Outline each blood parasite and name the species.
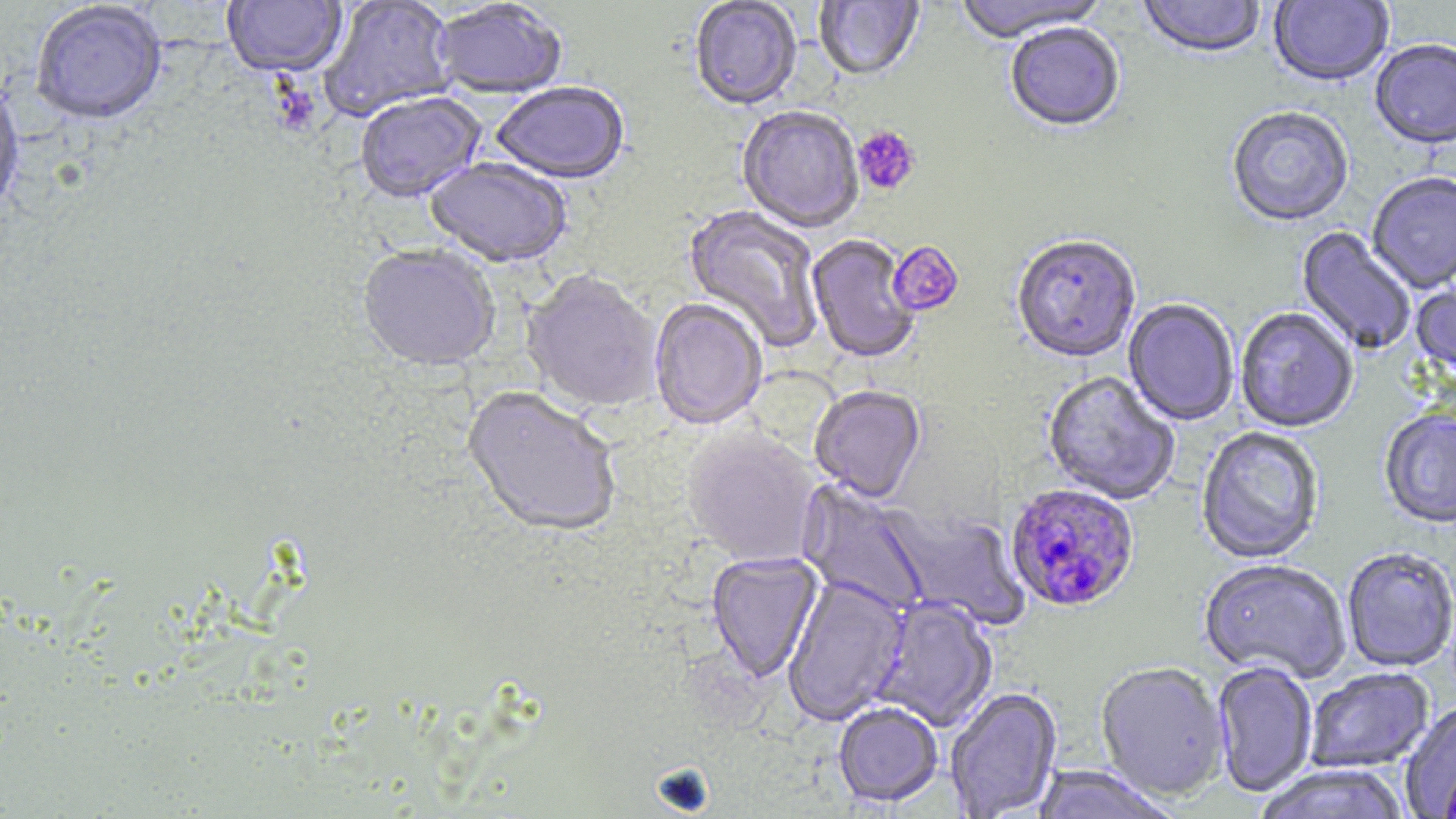

Approximate bounding boxes as (x1, y1, x2, y2) in pixels.
Plasmodium falciparum-infected red blood cells: (1004, 485, 1139, 613).
No Plasmodium ovale, Plasmodium malariae, Plasmodium vivax, Babesia divergens, or Trypanosoma brucei observed.

{
  "slide_level_diagnosis": "Plasmodium falciparum",
  "stain": "May-Grünwald-Giemsa",
  "modality": "optical microscopy",
  "platelet_locations": "approximate bounding boxes as (x1, y1, x2, y2) in pixels: (853, 126, 921, 196), (888, 241, 964, 318)",
  "image_size": "1456×819 pixels",
  "preparation": "thin blood smear",
  "field_of_view": "single",
  "uninfected_red_blood_cell_locations": "approximate bounding boxes as (x1, y1, x2, y2) in pixels: (221, 0, 347, 80), (319, 0, 457, 122), (689, 0, 802, 113), (952, 0, 1110, 45), (1138, 0, 1266, 61), (1269, 0, 1394, 89), (814, 1, 925, 83), (431, 2, 567, 102), (29, 3, 168, 127), (1005, 25, 1125, 135), (1370, 41, 1456, 152), (0, 75, 25, 222), (491, 84, 631, 186), (355, 93, 486, 205), (737, 107, 864, 235), (1226, 108, 1354, 228), (425, 160, 572, 270), (1367, 173, 1456, 295), (681, 205, 825, 352), (1296, 227, 1416, 356), (806, 235, 920, 365), (1011, 237, 1141, 365), (357, 247, 500, 376), (520, 272, 662, 416), (1411, 281, 1456, 381), (648, 300, 767, 432), (1122, 300, 1239, 426), (1235, 308, 1358, 435), (1042, 372, 1180, 507), (809, 387, 926, 504), (461, 388, 621, 541), (1379, 409, 1456, 531), (1195, 427, 1325, 565), (681, 430, 821, 569), (796, 480, 932, 617), (880, 506, 1030, 631), (1342, 548, 1456, 673), (707, 553, 825, 683), (1199, 561, 1350, 684), (783, 577, 910, 725), (870, 598, 999, 732), (1212, 662, 1319, 798), (1095, 663, 1231, 801), (1305, 668, 1434, 774), (945, 687, 1063, 819), (1400, 702, 1456, 818), (834, 703, 943, 808), (1253, 764, 1410, 819), (1030, 766, 1179, 819)",
  "magnification": "1000x"
}